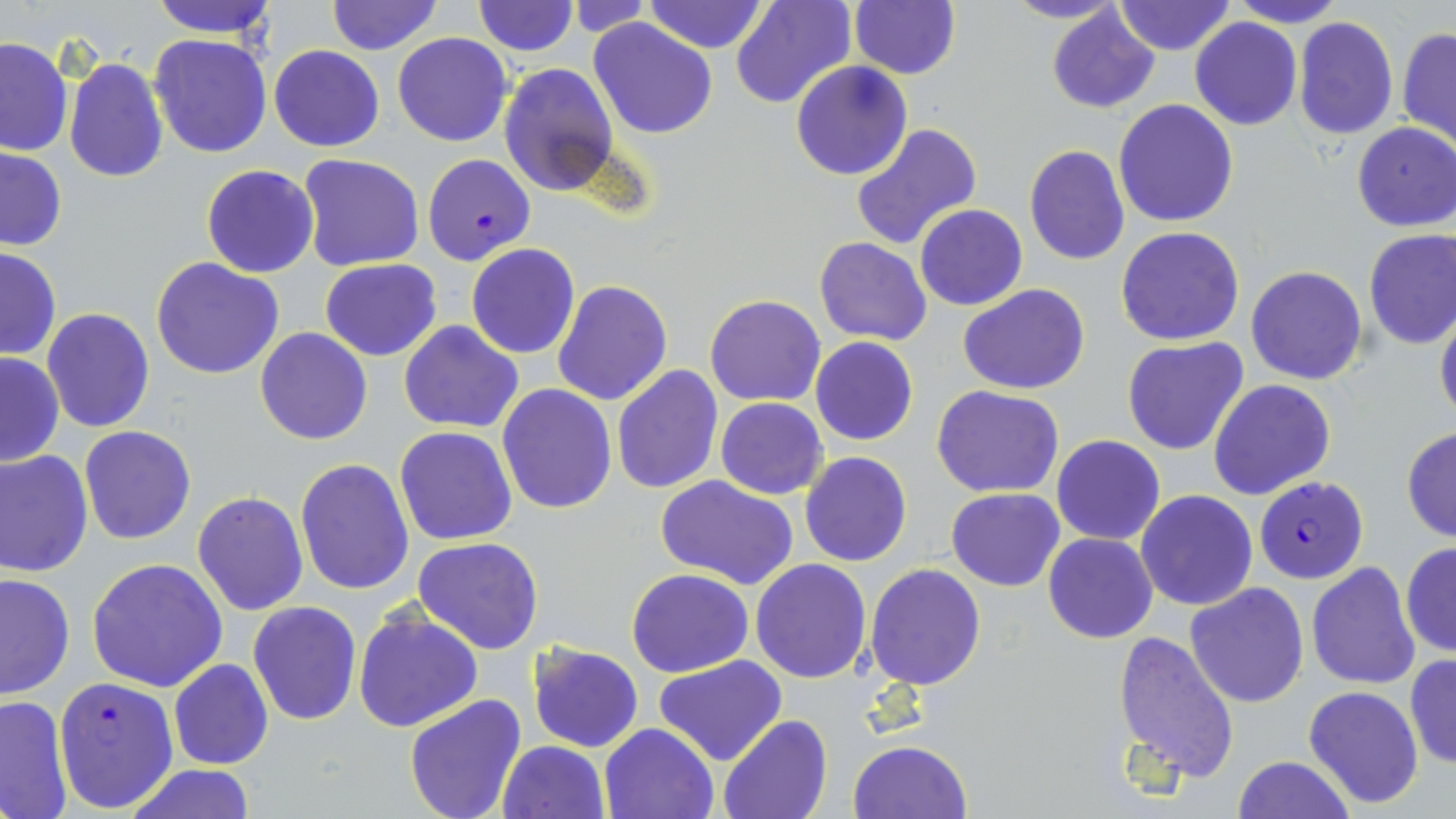

Summary:
  - Coordinate format: approximate bounding boxes as [x1, y1, x2, y2] in pixels
  - Uninfected red blood cell locations: [147, 0, 279, 38], [324, 0, 445, 55], [471, 0, 579, 56], [643, 0, 767, 54], [730, 0, 857, 109], [848, 0, 960, 80], [1002, 0, 1128, 24], [1112, 0, 1235, 56], [1227, 0, 1346, 28], [567, 1, 653, 38], [1045, 5, 1160, 113], [1292, 15, 1400, 141], [1190, 16, 1303, 130], [589, 17, 719, 139], [1398, 28, 1456, 150], [392, 31, 512, 146], [151, 34, 273, 157], [0, 37, 73, 157], [269, 45, 384, 152], [63, 57, 168, 184], [791, 60, 912, 181], [498, 63, 617, 195], [1113, 99, 1239, 229], [1351, 122, 1456, 231], [849, 123, 983, 250], [1023, 145, 1130, 266], [1, 146, 66, 251], [297, 154, 425, 273], [201, 163, 320, 277], [915, 204, 1027, 311], [1116, 227, 1246, 347], [1362, 228, 1456, 348], [813, 238, 932, 346], [466, 243, 580, 359], [0, 247, 61, 360], [151, 256, 284, 380], [320, 259, 442, 361], [1246, 265, 1366, 386], [552, 281, 672, 405], [959, 283, 1090, 396], [704, 295, 827, 405], [1434, 307, 1456, 426], [43, 308, 154, 431], [399, 321, 524, 434], [255, 328, 373, 445], [810, 336, 919, 446], [1122, 336, 1252, 456], [0, 350, 65, 468], [610, 366, 724, 497], [1207, 379, 1335, 501], [496, 384, 618, 515], [932, 385, 1063, 498], [717, 397, 828, 499], [80, 426, 197, 546], [394, 426, 517, 544], [1401, 427, 1456, 542], [1051, 435, 1165, 545], [0, 450, 94, 578], [799, 451, 913, 567], [293, 459, 414, 595], [654, 474, 799, 589], [946, 488, 1064, 592], [192, 490, 308, 614], [1135, 490, 1257, 611], [1042, 533, 1159, 643], [412, 536, 545, 656], [1400, 541, 1456, 658], [87, 557, 229, 691], [750, 558, 872, 683], [1306, 563, 1420, 689], [863, 564, 986, 689], [626, 569, 753, 677], [0, 571, 74, 700], [1185, 582, 1309, 706], [248, 602, 361, 725], [353, 609, 484, 733], [1113, 630, 1239, 783], [527, 641, 643, 751], [1405, 654, 1456, 770], [653, 655, 787, 765], [169, 659, 273, 769], [1303, 685, 1424, 808], [0, 695, 73, 818], [403, 695, 529, 819], [718, 714, 833, 819], [599, 721, 720, 819], [497, 740, 612, 819], [848, 740, 973, 819], [1233, 755, 1354, 819], [124, 763, 258, 819]
  - Plasmodium falciparum-infected red blood cell locations: [420, 153, 535, 265], [1254, 475, 1368, 584], [53, 676, 177, 812]
  - Slide-level diagnosis: Plasmodium falciparum
  - Modality: optical microscopy
  - Stain: May-Grünwald-Giemsa
  - Magnification: 1000x
  - Field of view: one of a larger specimen
  - Preparation: thin blood smear
  - Image size: 1456×819 pixels